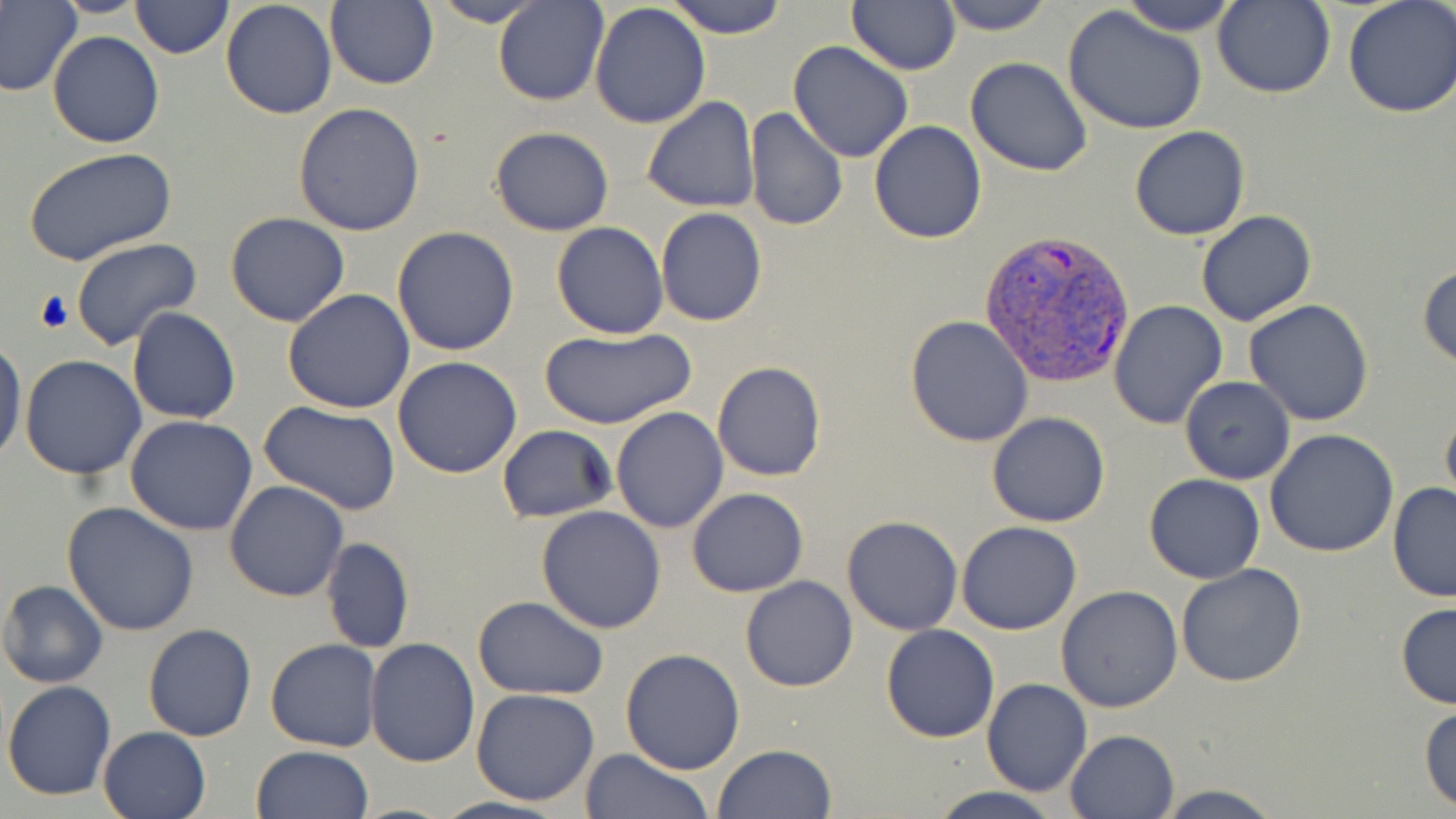 Approximate bounding boxes as (x1,y1)-(x2,y2) corner pairs in pixels. Plasmodium vivax-infected red blood cell locations: (977,230)-(1134,386). Uninfected red blood cell locations: (131,0)-(232,58), (493,0)-(608,107), (664,0)-(789,40), (847,0)-(961,76), (936,0)-(1053,35), (1116,0)-(1243,36), (1212,0)-(1334,98), (1343,0)-(1456,120), (0,1)-(80,98), (220,1)-(338,119), (426,1)-(546,27), (324,2)-(438,89), (589,3)-(711,129), (1062,5)-(1209,136), (47,31)-(164,148), (787,41)-(914,164), (965,56)-(1093,175), (642,97)-(760,213), (292,101)-(425,236), (744,108)-(848,232), (868,120)-(987,244), (1129,125)-(1251,241), (489,126)-(614,236), (23,145)-(176,266), (656,208)-(767,326), (1196,211)-(1319,327), (225,212)-(350,327), (552,221)-(669,338), (393,226)-(521,357), (71,237)-(203,350), (1417,262)-(1455,369), (283,289)-(416,413), (1109,299)-(1229,430), (1244,300)-(1375,426), (128,307)-(241,425), (905,314)-(1034,447), (537,327)-(696,429), (0,334)-(25,469), (20,354)-(147,480), (394,355)-(524,477), (712,360)-(826,482), (1180,377)-(1294,485), (259,402)-(403,516), (1441,404)-(1456,516), (611,406)-(728,534), (988,412)-(1111,527), (123,414)-(258,535), (497,425)-(616,523), (1266,428)-(1399,558), (1143,474)-(1266,584), (225,481)-(349,602), (1387,482)-(1456,600), (687,488)-(809,598), (62,502)-(199,636), (537,505)-(667,632), (841,515)-(964,635), (956,521)-(1082,635), (322,537)-(414,653), (1175,562)-(1307,686), (739,575)-(858,692), (1,579)-(108,688), (1056,586)-(1184,713), (472,596)-(608,699), (1395,602)-(1456,710), (143,623)-(257,743), (881,624)-(999,742), (266,638)-(380,752), (365,638)-(479,767), (621,648)-(747,775), (982,678)-(1092,797), (2,681)-(117,802), (471,689)-(600,806), (1419,702)-(1456,811), (97,726)-(211,819), (1065,728)-(1179,818), (713,744)-(836,819), (250,746)-(374,819), (579,748)-(714,819), (1154,784)-(1285,819), (928,787)-(1064,819), (430,797)-(569,819). Slide-level diagnosis: Plasmodium vivax. 1000x magnification. Light microscopy. One field of a larger specimen. Thin blood smear. Image is 1456×819 pixels. May-Grünwald-Giemsa-stained preparation.